Point out each Plasmodium parasite.
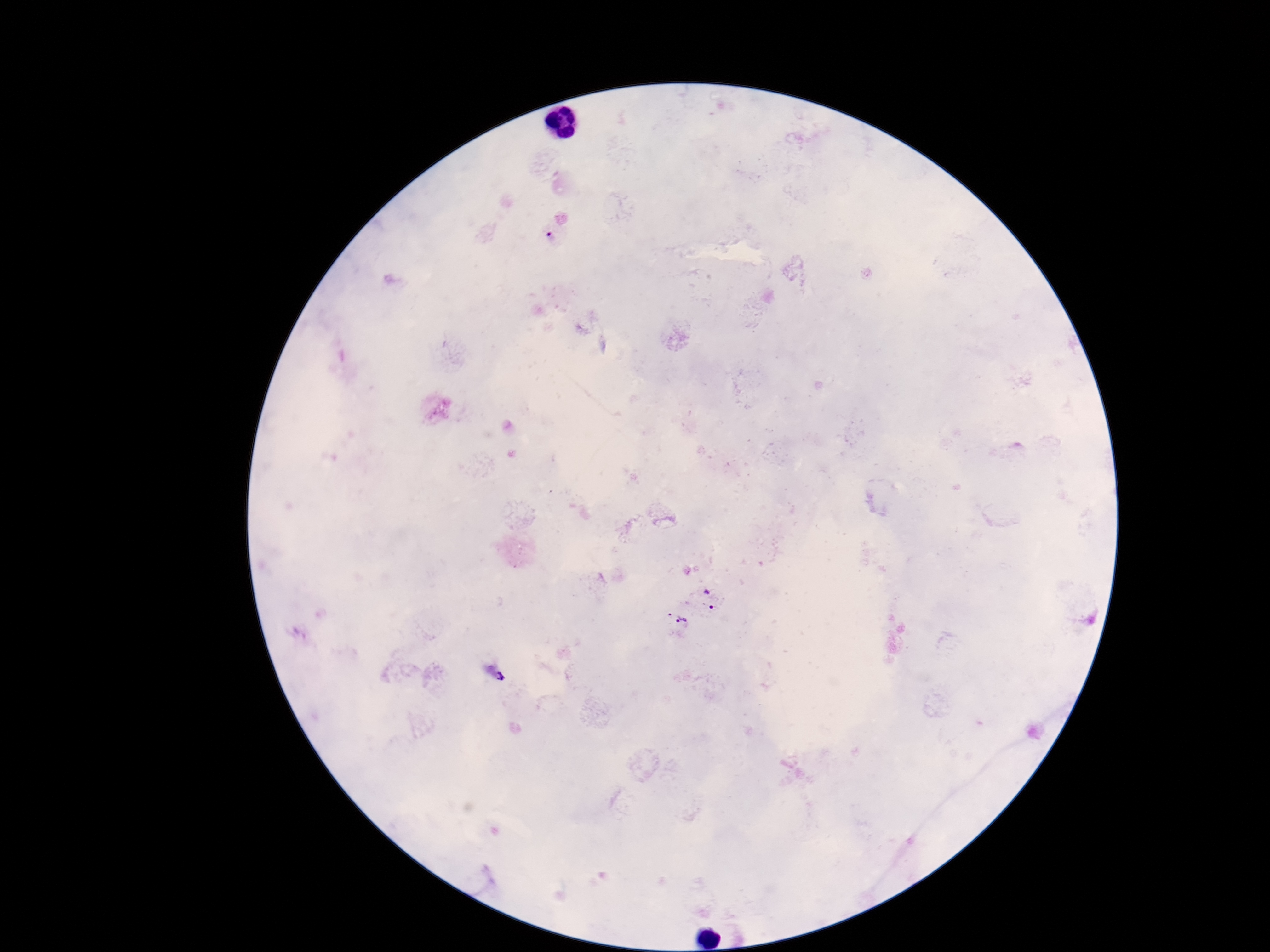
Approximate centers as {x, y} in pixels.
Plasmodium parasites: {555, 232}, {710, 599}, {678, 620}, {496, 674}.

field of view = single
stain = Giemsa
image size = 1270×952 pixels
magnification = 100x
patient malaria status = positive
capture = smartphone camera through the microscope eyepiece
preparation = thick peripheral-blood smear